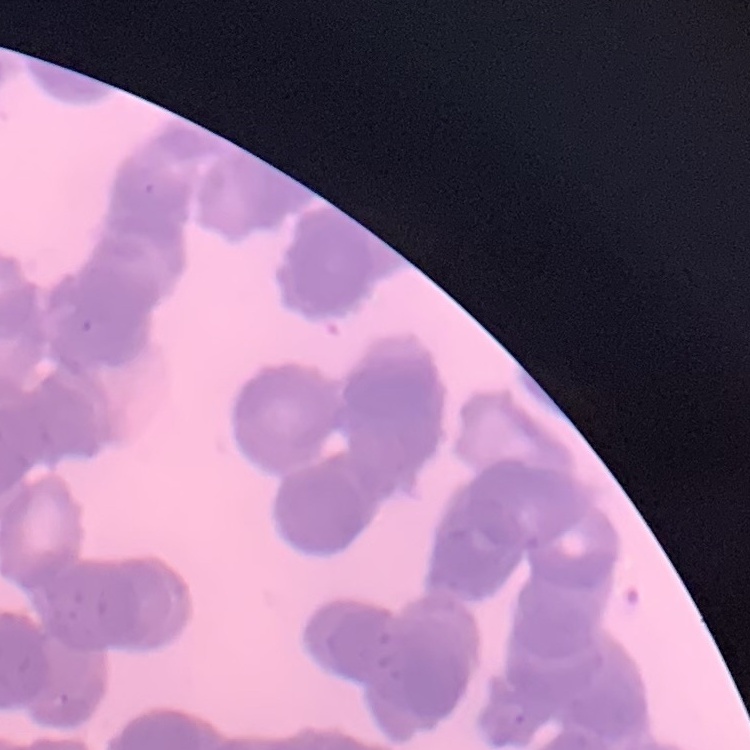
Summary:
  - Red blood cell morphology: rouleaux formation
  - Image type: one tile cut from a larger photomicrograph
  - Stain: Field's or Giemsa
  - Preparation: thin blood smear